Report the malaria status of this cell.
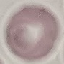
Uninfected.

Cell patch, automatically extracted from a larger field of view and resized to 64 × 64 pixels. Giemsa-stained preparation. Thin blood smear. Acquired by smartphone through the microscope eyepiece.